Name the parasite shown.
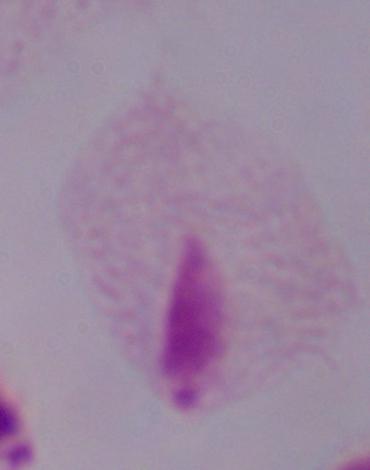
This is a trichomonad.

modality = photomicrograph
magnification = 1000x